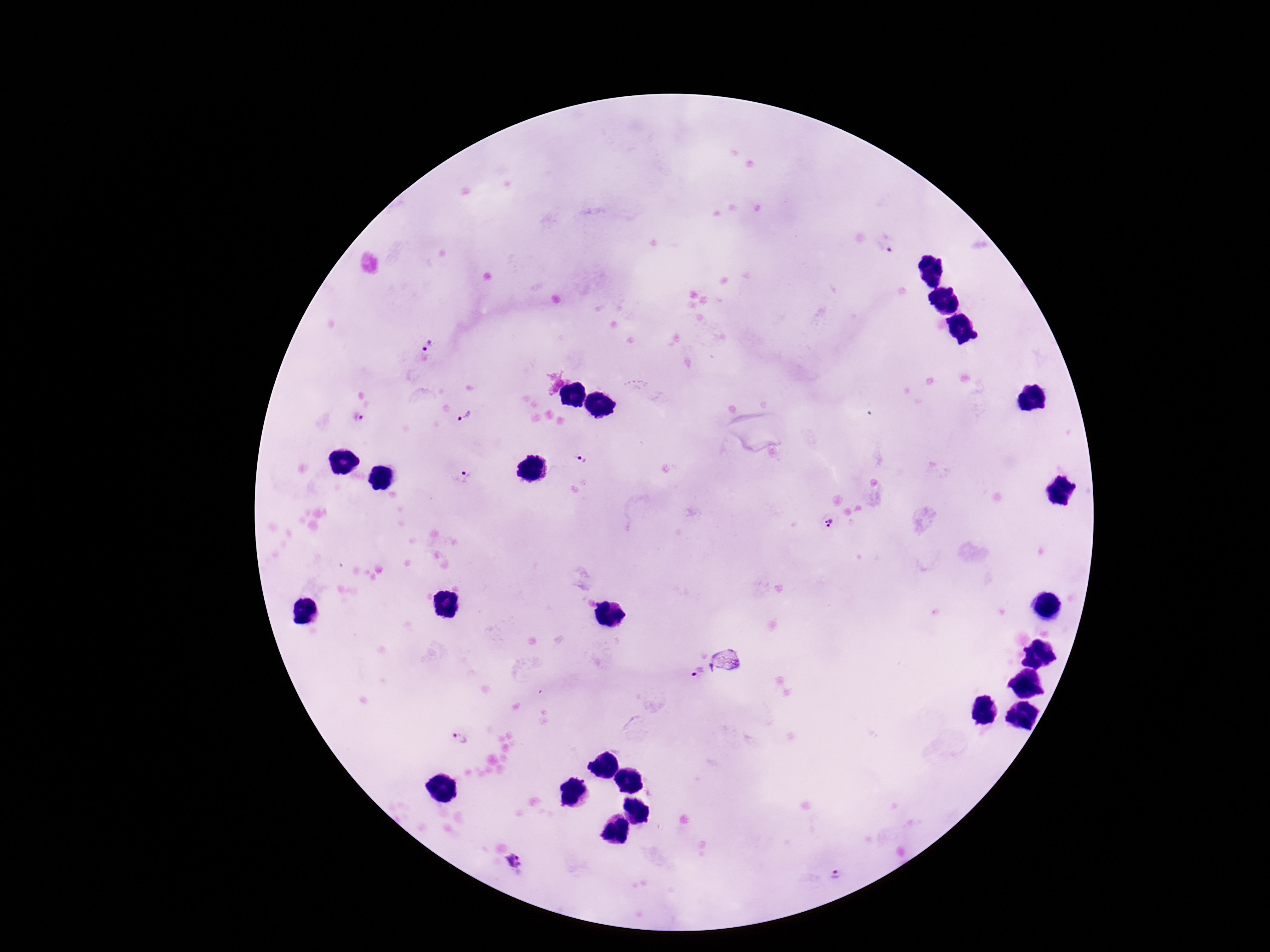

image_size: 1270×952 pixels
stain: Giemsa
capture: smartphone camera through the microscope eyepiece
magnification: 100x
field_of_view: single
patient_malaria_status: positive
preparation: thick blood film
plasmodium_parasite_locations: 'approximate object centers, in pixels from the top-left corner: (x=886, y=246), (x=427, y=346), (x=358, y=417), (x=466, y=417), (x=581, y=460), (x=466, y=476), (x=829, y=521), (x=729, y=660), (x=697, y=675), (x=460, y=738), (x=515, y=860), (x=835, y=876)'